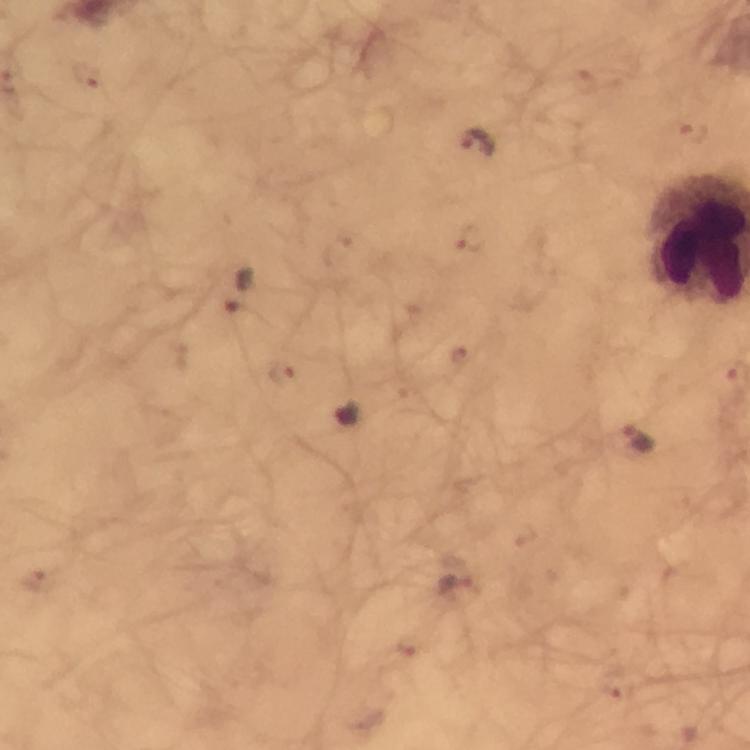
context: from a malaria diagnostic workup
preparation: thick blood smear
capture: smartphone mounted on the microscope
immersion_oil: used
plasmodium_parasite_locations: 'approximate object centers, in pixels from the top-left corner: (x=84, y=74), (x=584, y=79), (x=690, y=133), (x=475, y=145), (x=471, y=239), (x=242, y=292), (x=462, y=356), (x=282, y=374), (x=637, y=437), (x=37, y=581), (x=456, y=582), (x=412, y=645), (x=617, y=681)'
stain: Giemsa
image_size: 750×750 pixels
cropped_from: one field of view
magnification: 100x